Comment on the morphology of the erythrocytes.
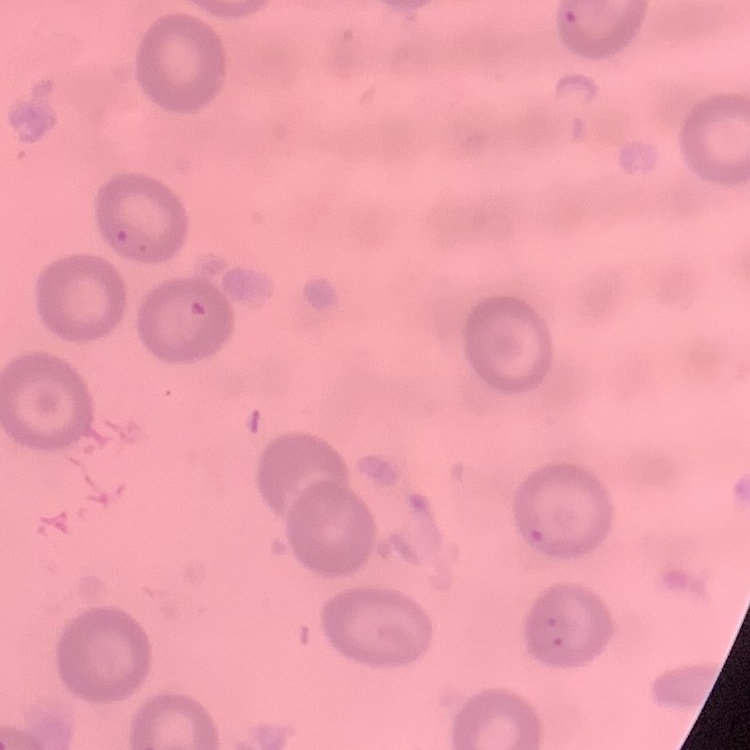

They show no rouleaux formation.

Field's or Giemsa stain. Thin blood smear. One tile cut from a larger photomicrograph.